State which parasite is depicted.
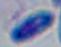

Toxoplasma gondii.

modality: micrograph
magnification: 1000x